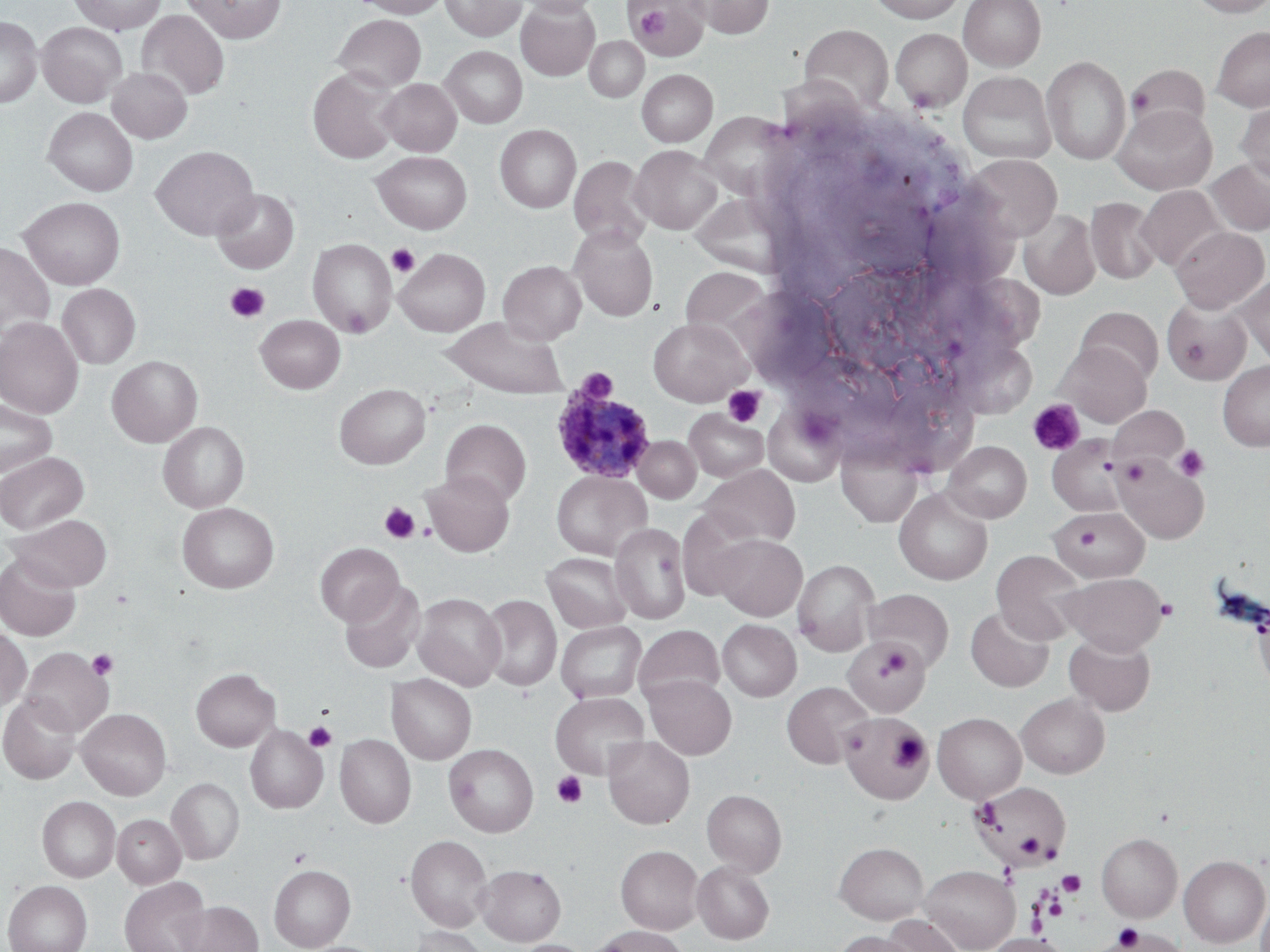
Approximate bounding boxes as named x1/y1/x2/y2 corners in pixels. Uninfected red blood cell locations (subset): (x1=69, y1=0, x2=166, y2=34), (x1=182, y1=0, x2=286, y2=42), (x1=353, y1=0, x2=447, y2=18), (x1=439, y1=0, x2=526, y2=41), (x1=516, y1=0, x2=600, y2=17), (x1=690, y1=0, x2=774, y2=38), (x1=866, y1=0, x2=967, y2=22), (x1=958, y1=0, x2=1045, y2=70), (x1=1186, y1=0, x2=1270, y2=17), (x1=516, y1=1, x2=600, y2=80), (x1=629, y1=1, x2=708, y2=60), (x1=136, y1=9, x2=229, y2=101), (x1=333, y1=14, x2=426, y2=91), (x1=0, y1=16, x2=42, y2=107), (x1=37, y1=22, x2=127, y2=107), (x1=799, y1=23, x2=893, y2=113), (x1=1212, y1=25, x2=1270, y2=112), (x1=890, y1=28, x2=971, y2=112), (x1=585, y1=36, x2=649, y2=102), (x1=440, y1=46, x2=527, y2=128), (x1=1042, y1=55, x2=1131, y2=165), (x1=1126, y1=64, x2=1211, y2=139), (x1=107, y1=67, x2=192, y2=143), (x1=308, y1=67, x2=400, y2=164), (x1=636, y1=69, x2=717, y2=146), (x1=958, y1=71, x2=1057, y2=164), (x1=378, y1=79, x2=461, y2=156), (x1=1235, y1=100, x2=1270, y2=187), (x1=1112, y1=104, x2=1216, y2=194), (x1=43, y1=107, x2=138, y2=196), (x1=699, y1=113, x2=790, y2=198), (x1=495, y1=124, x2=581, y2=213), (x1=150, y1=145, x2=258, y2=241), (x1=630, y1=145, x2=722, y2=233), (x1=371, y1=151, x2=472, y2=234), (x1=965, y1=154, x2=1061, y2=242), (x1=569, y1=155, x2=653, y2=246), (x1=1207, y1=158, x2=1270, y2=235), (x1=1136, y1=185, x2=1228, y2=272), (x1=212, y1=189, x2=299, y2=273), (x1=690, y1=193, x2=784, y2=274), (x1=19, y1=197, x2=125, y2=289), (x1=1086, y1=197, x2=1161, y2=284), (x1=1019, y1=209, x2=1100, y2=300), (x1=568, y1=224, x2=658, y2=321), (x1=1170, y1=225, x2=1269, y2=313), (x1=308, y1=238, x2=397, y2=337), (x1=0, y1=242, x2=55, y2=339), (x1=498, y1=260, x2=586, y2=345), (x1=681, y1=266, x2=771, y2=342), (x1=1235, y1=276, x2=1270, y2=367), (x1=57, y1=284, x2=141, y2=369), (x1=1163, y1=298, x2=1252, y2=384), (x1=1076, y1=307, x2=1163, y2=385), (x1=255, y1=315, x2=345, y2=393), (x1=0, y1=317, x2=84, y2=418), (x1=439, y1=317, x2=569, y2=398), (x1=648, y1=317, x2=752, y2=406), (x1=1057, y1=342, x2=1152, y2=427), (x1=107, y1=355, x2=202, y2=447), (x1=1218, y1=361, x2=1270, y2=451), (x1=334, y1=383, x2=430, y2=469), (x1=0, y1=398, x2=57, y2=478), (x1=1108, y1=405, x2=1189, y2=467), (x1=684, y1=408, x2=767, y2=482), (x1=441, y1=418, x2=531, y2=508), (x1=158, y1=422, x2=249, y2=512), (x1=633, y1=436, x2=701, y2=503), (x1=836, y1=437, x2=924, y2=528), (x1=1047, y1=437, x2=1124, y2=516), (x1=944, y1=441, x2=1031, y2=523), (x1=0, y1=452, x2=88, y2=534), (x1=1113, y1=454, x2=1209, y2=544), (x1=698, y1=465, x2=801, y2=548), (x1=422, y1=470, x2=514, y2=556), (x1=551, y1=471, x2=652, y2=560), (x1=894, y1=488, x2=992, y2=585), (x1=177, y1=502, x2=279, y2=593), (x1=1049, y1=506, x2=1148, y2=582), (x1=6, y1=514, x2=113, y2=592), (x1=610, y1=523, x2=690, y2=624), (x1=713, y1=534, x2=806, y2=620), (x1=315, y1=543, x2=403, y2=626), (x1=991, y1=550, x2=1088, y2=644), (x1=542, y1=552, x2=632, y2=633), (x1=0, y1=554, x2=81, y2=641), (x1=792, y1=559, x2=880, y2=656), (x1=1059, y1=572, x2=1168, y2=654), (x1=339, y1=579, x2=425, y2=674), (x1=864, y1=588, x2=954, y2=671), (x1=413, y1=593, x2=505, y2=690), (x1=479, y1=594, x2=561, y2=691), (x1=966, y1=606, x2=1054, y2=692), (x1=718, y1=620, x2=801, y2=701), (x1=555, y1=621, x2=647, y2=703), (x1=634, y1=625, x2=725, y2=705), (x1=0, y1=627, x2=31, y2=711), (x1=1064, y1=634, x2=1155, y2=716), (x1=843, y1=639, x2=931, y2=717), (x1=20, y1=646, x2=113, y2=736), (x1=191, y1=668, x2=280, y2=751), (x1=386, y1=673, x2=477, y2=764), (x1=645, y1=675, x2=736, y2=759), (x1=782, y1=681, x2=873, y2=768), (x1=550, y1=692, x2=649, y2=778), (x1=1016, y1=693, x2=1109, y2=778), (x1=1, y1=695, x2=81, y2=783), (x1=76, y1=708, x2=171, y2=800), (x1=839, y1=712, x2=930, y2=805), (x1=933, y1=712, x2=1026, y2=803), (x1=246, y1=725, x2=327, y2=814), (x1=335, y1=734, x2=416, y2=828), (x1=602, y1=735, x2=694, y2=828), (x1=444, y1=744, x2=538, y2=837), (x1=167, y1=777, x2=244, y2=864), (x1=972, y1=782, x2=1070, y2=865), (x1=702, y1=789, x2=786, y2=875), (x1=37, y1=796, x2=120, y2=882), (x1=113, y1=814, x2=186, y2=888), (x1=1097, y1=832, x2=1182, y2=922), (x1=405, y1=834, x2=493, y2=931), (x1=834, y1=842, x2=929, y2=924), (x1=616, y1=845, x2=703, y2=934), (x1=1179, y1=855, x2=1269, y2=947), (x1=692, y1=860, x2=774, y2=944), (x1=269, y1=864, x2=355, y2=951), (x1=475, y1=864, x2=565, y2=945), (x1=920, y1=865, x2=1020, y2=951), (x1=119, y1=877, x2=210, y2=952), (x1=3, y1=880, x2=92, y2=952), (x1=1256, y1=889, x2=1270, y2=952), (x1=177, y1=900, x2=263, y2=952), (x1=881, y1=914, x2=966, y2=952), (x1=408, y1=926, x2=492, y2=952), (x1=590, y1=926, x2=690, y2=952), (x1=1118, y1=927, x2=1188, y2=951), (x1=833, y1=930, x2=921, y2=952), (x1=987, y1=933, x2=1066, y2=951), (x1=509, y1=939, x2=594, y2=952). Platelet locations (subset): (x1=633, y1=6, x2=672, y2=41), (x1=1127, y1=89, x2=1153, y2=114), (x1=387, y1=244, x2=419, y2=277), (x1=225, y1=282, x2=269, y2=323), (x1=342, y1=306, x2=372, y2=337), (x1=575, y1=367, x2=617, y2=402), (x1=723, y1=385, x2=766, y2=427), (x1=1028, y1=399, x2=1086, y2=455), (x1=1173, y1=445, x2=1209, y2=482), (x1=1120, y1=459, x2=1149, y2=485), (x1=380, y1=502, x2=420, y2=544), (x1=1155, y1=597, x2=1178, y2=620), (x1=844, y1=639, x2=928, y2=714), (x1=879, y1=647, x2=911, y2=677), (x1=87, y1=649, x2=118, y2=679), (x1=304, y1=722, x2=336, y2=751), (x1=890, y1=732, x2=929, y2=771), (x1=552, y1=772, x2=588, y2=808), (x1=1016, y1=833, x2=1045, y2=858), (x1=1058, y1=871, x2=1085, y2=896), (x1=1045, y1=896, x2=1068, y2=920), (x1=1114, y1=924, x2=1144, y2=950). Plasmodium ovale-infected red blood cell locations: (x1=554, y1=391, x2=658, y2=484). Slide-level diagnosis: Plasmodium ovale. May-Grünwald-Giemsa stain. Image is 1270×952 pixels. Thin blood smear. Light microscopy. Single field of view. Captured at 1000x magnification.